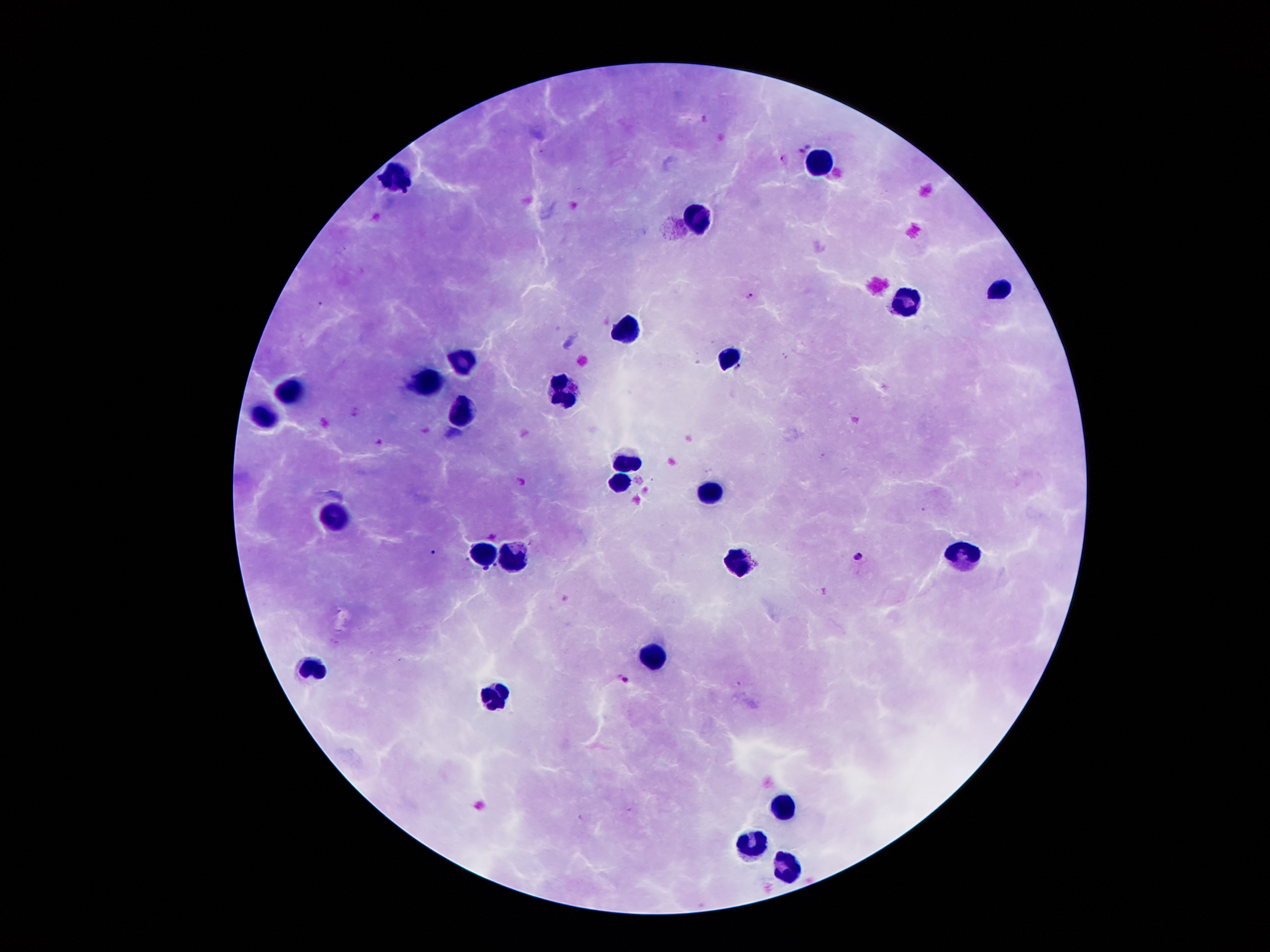
{
  "leukocyte_locations": "approximate object centers, in pixels from the top-left corner: (x=822, y=164), (x=398, y=177), (x=696, y=215), (x=1002, y=292), (x=907, y=302), (x=633, y=333), (x=728, y=360), (x=463, y=361), (x=427, y=383), (x=294, y=390), (x=563, y=390), (x=467, y=412), (x=262, y=421), (x=628, y=462), (x=621, y=486), (x=712, y=491), (x=335, y=520), (x=483, y=553), (x=962, y=556), (x=517, y=559), (x=742, y=563), (x=656, y=657), (x=316, y=667), (x=495, y=697), (x=782, y=808), (x=753, y=846), (x=783, y=870)",
  "stain": "Giemsa",
  "malaria_parasite_locations": "approximate object centers, in pixels from the top-left corner: (x=801, y=150), (x=781, y=159), (x=749, y=295), (x=320, y=303), (x=432, y=551), (x=858, y=557), (x=486, y=568), (x=625, y=680)",
  "preparation": "thick blood film",
  "field_of_view": "single",
  "patient_malaria_status": "positive for Plasmodium falciparum",
  "magnification": "100x",
  "capture": "smartphone through the microscope eyepiece",
  "image_size": "1270×952 pixels"
}